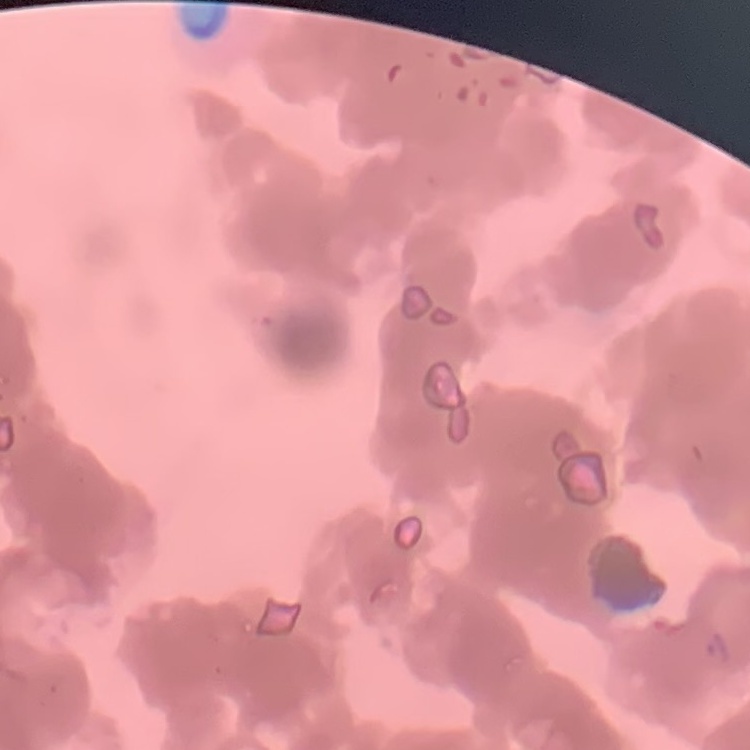
The red blood cells show rouleaux formation. Field's or Giemsa stain. One tile cut from a larger photomicrograph. Thin peripheral smear.